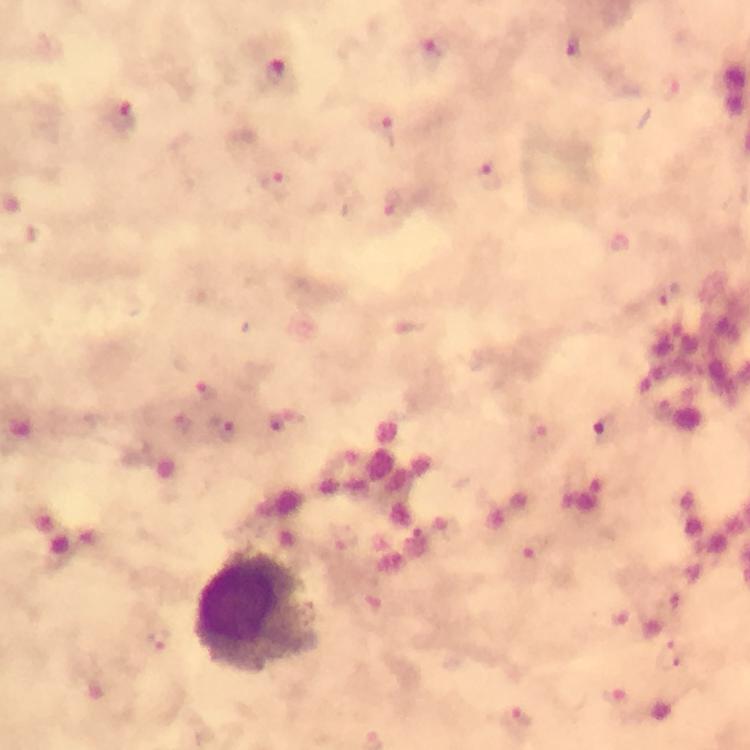

Approximate centers as (x, y) in pixels. Malaria parasite locations: (437, 46), (573, 48), (277, 74), (122, 116), (387, 129), (488, 178), (276, 185), (388, 204), (656, 299), (205, 391), (183, 423), (223, 431), (604, 431), (535, 550), (621, 620), (160, 640), (668, 656), (616, 700), (519, 717). Leukocyte locations: (257, 611). Giemsa stain. Thick blood smear. Immersion oil was used. From a malaria diagnostic workup. 100x magnification. Photographed with a smartphone mounted on the microscope. Image is 750×750 pixels. Cropped region of a single field of view.